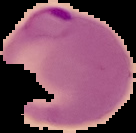

Summary:
  - Preparation: thin blood film
  - Image size: 136×133 pixels
  - Result: malaria parasites detected
  - Image type: segmented cell region with the area outside set to black